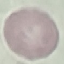
malaria status = uninfected
capture = smartphone through the microscope eyepiece
image type = cell patch, automatically extracted from a larger field of view and resized to 64 × 64 pixels
preparation = thin blood film
stain = Giemsa